Assess this cell for malaria.
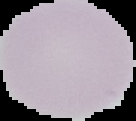

It is uninfected.

From a thin blood film. Cell region segmented out of the field of view; the surrounding area is masked to black. Image is 136×121 pixels.